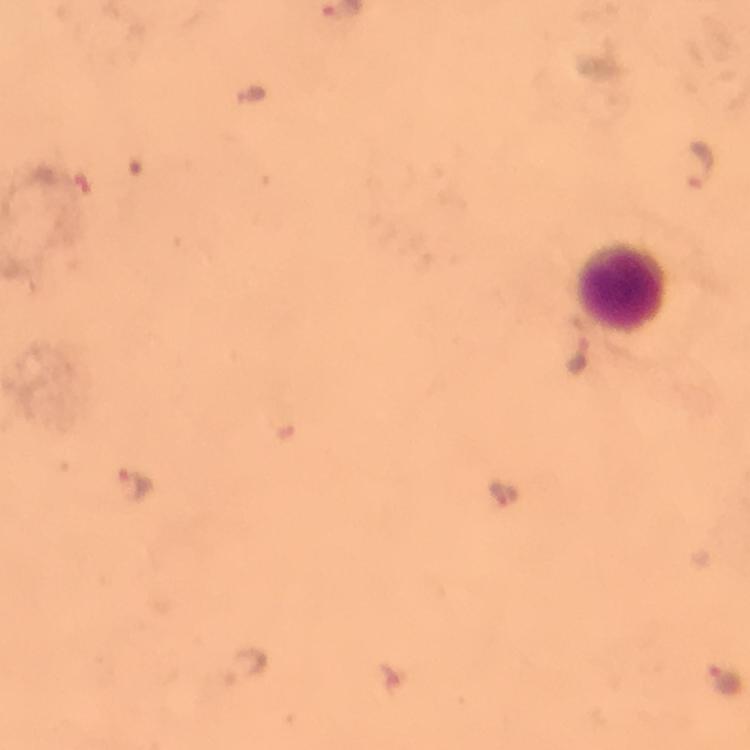
Approximate object centers, in pixels from the top-left corner. Malaria parasite locations: (x=254, y=95), (x=702, y=163), (x=579, y=360), (x=134, y=486), (x=503, y=490), (x=246, y=668), (x=726, y=676). Leukocyte locations: (x=620, y=288). Photographed with a smartphone mounted on the microscope. Immersion oil was used. 100x magnification. From a diagnostic examination for malaria. Thick blood film. Giemsa stain. A crop from one field of view. Image is 750×750 pixels.